Identify the blood parasite species.
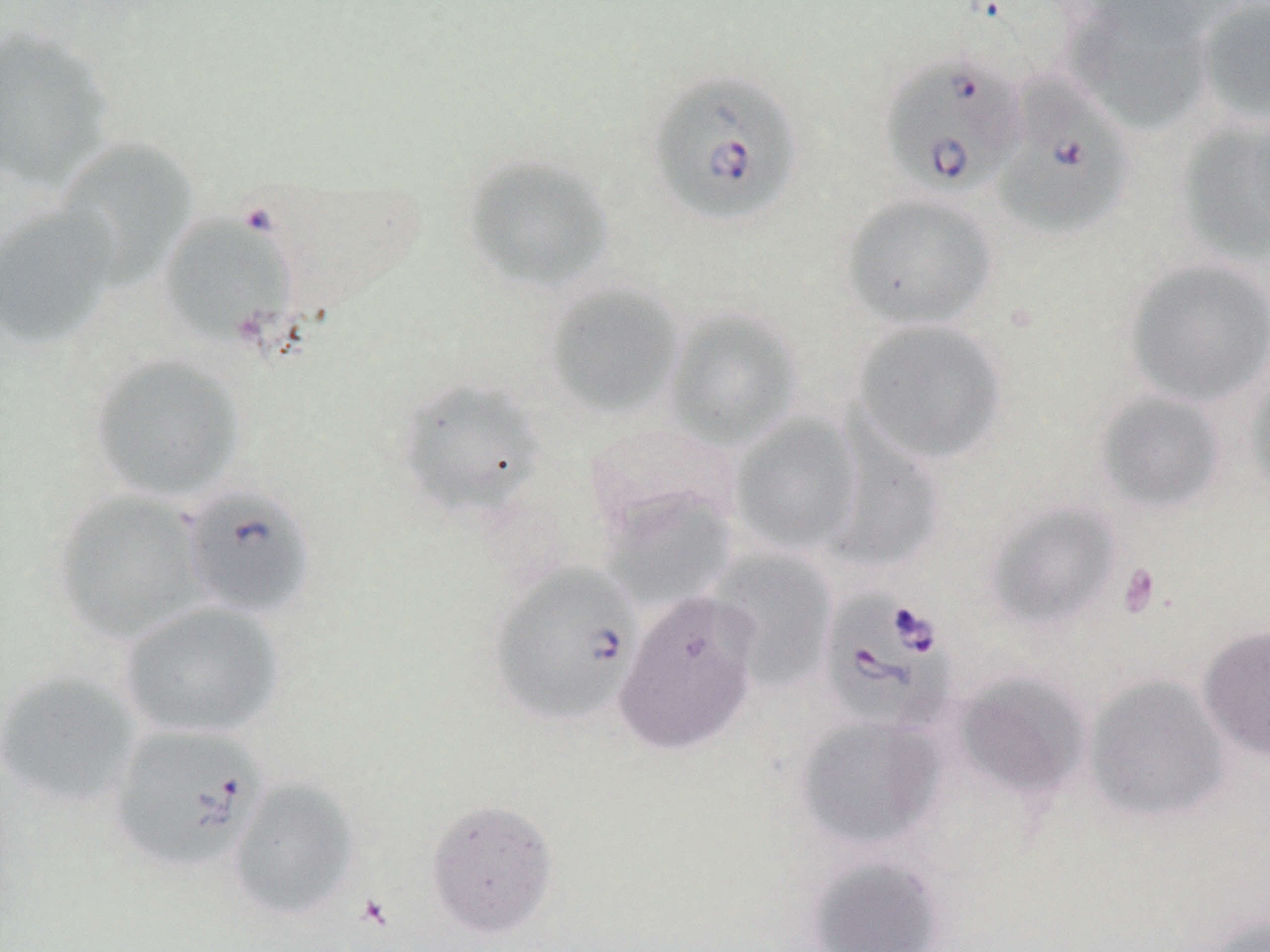
Babesia divergens.

modality = optical microscopy
platelet locations = approximate bounding boxes as [x1, y1, x2, y2] in pixels: [1118, 563, 1161, 618]
preparation = thin blood smear
stain = May-Grünwald-Giemsa
uninfected red blood cell locations = approximate bounding boxes as [x1, y1, x2, y2] in pixels: [1060, 1, 1215, 136], [1197, 1, 1270, 125], [0, 26, 116, 190], [1176, 117, 1270, 265], [54, 137, 198, 286], [463, 155, 615, 293], [840, 193, 998, 330], [0, 204, 120, 350], [159, 213, 297, 347], [1124, 258, 1270, 406], [544, 283, 685, 419], [663, 307, 803, 450], [852, 319, 1009, 465], [88, 353, 246, 503], [1244, 363, 1270, 510], [393, 377, 547, 519], [1094, 390, 1228, 513], [729, 414, 863, 556], [823, 418, 945, 575], [51, 490, 208, 643], [602, 491, 735, 612], [984, 501, 1122, 631], [708, 549, 837, 691], [614, 590, 762, 757], [119, 601, 285, 740], [1198, 625, 1270, 760], [0, 669, 142, 809], [952, 670, 1090, 801], [1083, 674, 1231, 825], [794, 714, 946, 853], [228, 777, 360, 921], [425, 798, 559, 939], [805, 854, 945, 952], [1199, 913, 1270, 952]
magnification = 1000x
field of view = single
Babesia divergens-infected red blood cell locations = approximate bounding boxes as [x1, y1, x2, y2] in pixels: [878, 52, 1026, 199], [648, 70, 803, 227], [993, 76, 1134, 239], [180, 485, 316, 619], [488, 562, 642, 727], [817, 586, 960, 736], [107, 722, 269, 873]
image size = 1270×952 pixels